Outline each Plasmodium falciparum-infected red blood cell.
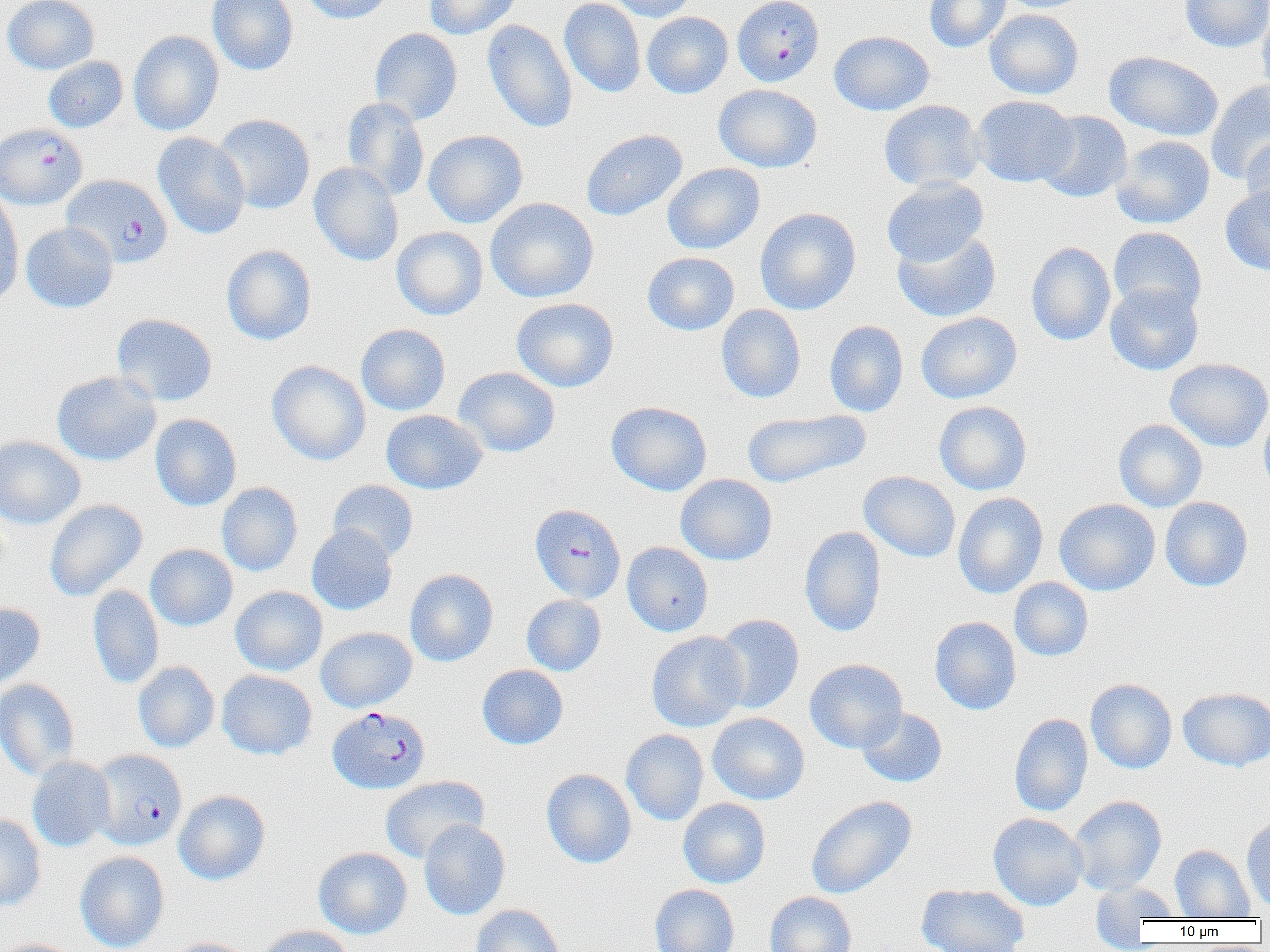

Approximate bounding boxes as (x1, y1, x2, y2) in pixels.
Plasmodium falciparum-infected red blood cells: (732, 0, 824, 87), (0, 124, 87, 210), (63, 174, 172, 267), (529, 503, 626, 603), (327, 706, 430, 795), (90, 749, 186, 850).

Summary:
  - Uninfected red blood cell locations: (2, 0, 99, 75), (207, 0, 298, 76), (299, 0, 393, 24), (424, 0, 522, 39), (559, 0, 646, 97), (608, 0, 697, 22), (924, 0, 1011, 52), (997, 0, 1091, 13), (1180, 0, 1270, 52), (1256, 7, 1270, 103), (984, 9, 1083, 99), (642, 11, 733, 98), (483, 19, 577, 134), (369, 28, 462, 125), (128, 30, 224, 136), (830, 30, 934, 116), (1104, 50, 1224, 142), (43, 56, 128, 133), (1206, 81, 1270, 185), (713, 84, 822, 172), (971, 95, 1077, 187), (341, 97, 430, 200), (879, 99, 984, 192), (1035, 111, 1132, 203), (212, 114, 315, 215), (423, 129, 528, 228), (581, 129, 687, 221), (153, 132, 250, 239), (1111, 135, 1215, 229), (1241, 135, 1270, 226), (308, 162, 404, 266), (662, 162, 764, 254), (881, 178, 988, 267), (1220, 186, 1270, 275), (0, 190, 24, 307), (485, 197, 599, 303), (755, 207, 861, 315), (21, 222, 117, 313), (392, 226, 488, 320), (1108, 227, 1207, 318), (892, 229, 1001, 323), (1026, 242, 1116, 346), (221, 245, 316, 346), (642, 252, 739, 336), (1104, 282, 1203, 376), (511, 297, 619, 393), (716, 305, 806, 403), (916, 312, 1022, 403), (112, 313, 218, 406), (824, 320, 909, 417), (356, 324, 450, 415), (1166, 358, 1270, 452), (267, 360, 370, 465), (453, 366, 560, 457), (51, 371, 161, 466), (605, 401, 712, 496), (933, 401, 1032, 495), (1258, 406, 1270, 499), (381, 409, 487, 494), (742, 409, 871, 488), (150, 414, 241, 511), (1113, 419, 1207, 511), (0, 435, 86, 529), (858, 471, 960, 562), (675, 474, 777, 565), (327, 480, 418, 562), (216, 482, 303, 577), (952, 492, 1048, 599), (1160, 497, 1253, 592), (1054, 498, 1161, 596), (44, 499, 148, 601), (306, 524, 398, 615), (799, 526, 887, 637), (621, 542, 713, 636), (145, 544, 238, 631), (405, 569, 498, 667), (1009, 577, 1094, 661), (88, 584, 164, 689), (231, 586, 328, 676), (522, 595, 606, 676), (0, 603, 45, 690), (711, 613, 804, 713), (930, 616, 1021, 715), (315, 626, 417, 712), (646, 631, 748, 732), (804, 659, 908, 753), (133, 661, 220, 752), (477, 665, 568, 749), (216, 669, 317, 759), (0, 678, 80, 781), (1085, 678, 1177, 773), (1178, 687, 1270, 771), (857, 707, 947, 788), (707, 712, 810, 805), (1009, 713, 1093, 817), (621, 729, 709, 825), (27, 756, 115, 852), (541, 769, 636, 868), (380, 775, 489, 863), (173, 790, 271, 885), (805, 795, 917, 899), (1069, 795, 1167, 894), (678, 798, 770, 888), (988, 812, 1088, 911), (0, 813, 46, 913), (1241, 814, 1270, 914), (418, 819, 510, 920), (1170, 844, 1255, 920), (313, 847, 412, 939), (74, 851, 169, 952), (1091, 879, 1180, 931), (917, 883, 1029, 952), (650, 884, 739, 952), (765, 892, 857, 952), (470, 904, 566, 952), (257, 925, 354, 952), (166, 937, 257, 952), (0, 938, 80, 952)
  - Slide-level diagnosis: Plasmodium falciparum
  - Magnification: 1000x
  - Field of view: single
  - Preparation: thin blood film
  - Modality: optical microscopy
  - Image size: 1270×952 pixels